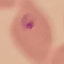

Result: malaria parasites detected. Cell patch, automatically extracted from a larger field of view and resized to 64 × 64 pixels. Giemsa-stained preparation. Acquired by smartphone through the microscope eyepiece. Thin blood film.